Classify this cell by malaria status.
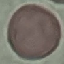

Uninfected.

image type = cell patch, automatically extracted from a larger field of view and resized to 64 × 64 pixels
preparation = thin blood smear
stain = Giemsa
capture = smartphone camera at the microscope eyepiece